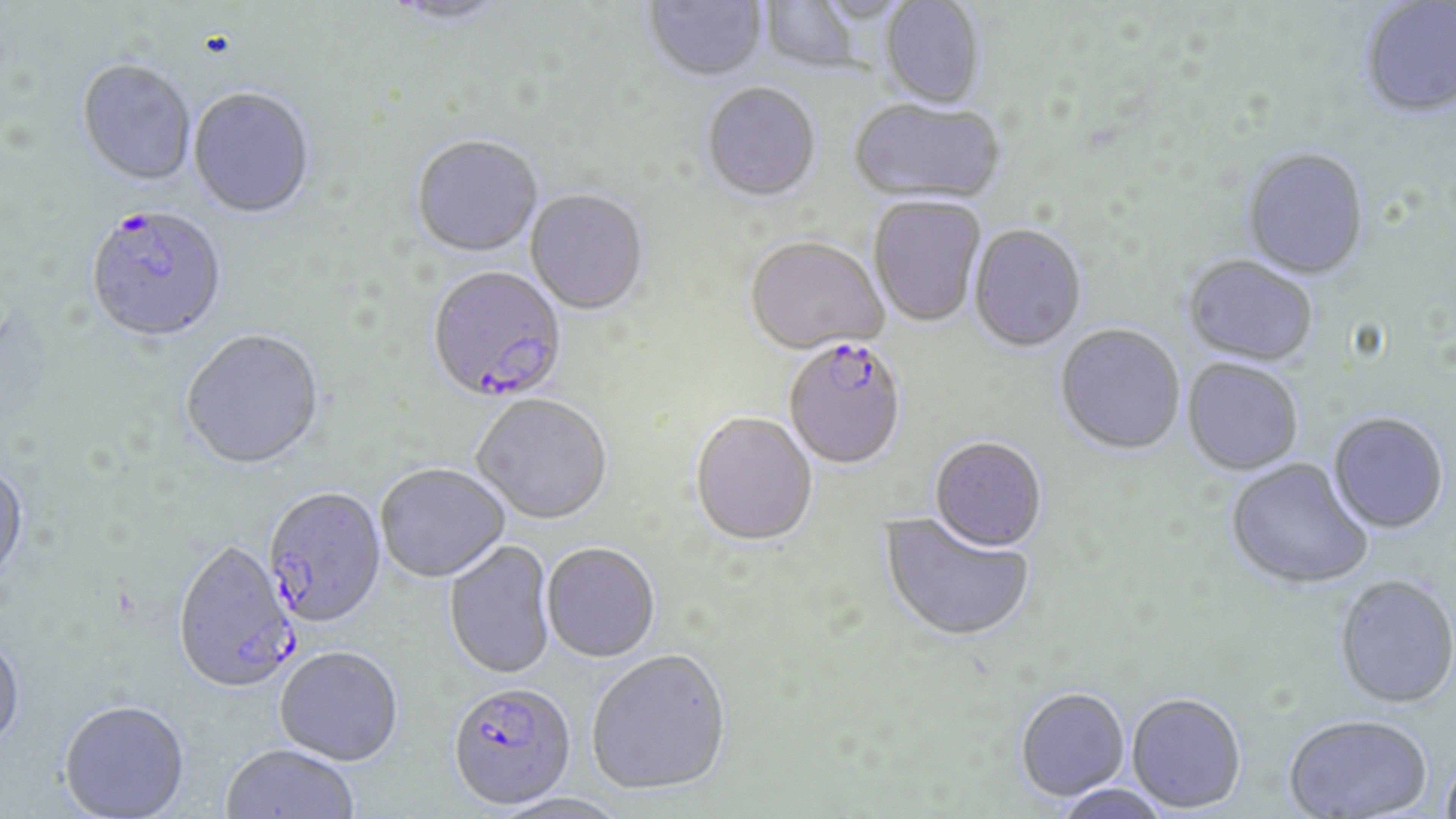

Approximate bounding boxes as (x1, y1, x2, y2) in pixels. Plasmodium falciparum-infected red blood cell locations: (85, 207, 228, 344), (429, 265, 570, 401), (783, 341, 907, 472), (262, 489, 387, 630), (172, 543, 300, 698), (448, 688, 578, 815). Uninfected red blood cell locations: (382, 0, 512, 28), (643, 0, 768, 85), (759, 0, 864, 75), (1360, 0, 1456, 120), (879, 1, 985, 109), (76, 61, 196, 189), (702, 85, 821, 204), (188, 89, 316, 221), (849, 101, 1005, 206), (411, 136, 545, 259), (1241, 150, 1370, 282), (525, 191, 649, 317), (868, 197, 986, 329), (969, 225, 1087, 354), (745, 239, 888, 358), (1182, 257, 1318, 368), (1055, 325, 1185, 457), (179, 332, 327, 473), (1182, 360, 1303, 477), (472, 396, 612, 527), (689, 414, 817, 549), (1328, 415, 1449, 536), (929, 438, 1047, 555), (1226, 459, 1373, 591), (0, 464, 29, 586), (376, 466, 509, 585), (877, 511, 1036, 645), (444, 541, 556, 682), (541, 545, 661, 665), (1333, 577, 1456, 711), (0, 634, 26, 755), (274, 649, 403, 769), (587, 653, 732, 799), (1015, 689, 1130, 803), (1126, 694, 1247, 815), (58, 703, 191, 819), (1283, 716, 1432, 818), (220, 746, 358, 819), (1439, 755, 1456, 818), (1052, 784, 1172, 819), (493, 795, 631, 819). Slide-level diagnosis: Plasmodium falciparum. Image is 1456×819 pixels. Single field of view. Thin blood smear. 1000x magnification. Light microscopy. May-Grünwald-Giemsa stain.